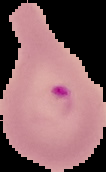

Summary:
  - Preparation: thin blood film
  - Image size: 106×172 pixels
  - Image type: segmented cell region with the area outside set to black
  - Result: malaria parasites detected